Locate every blood parasite and identify its species.
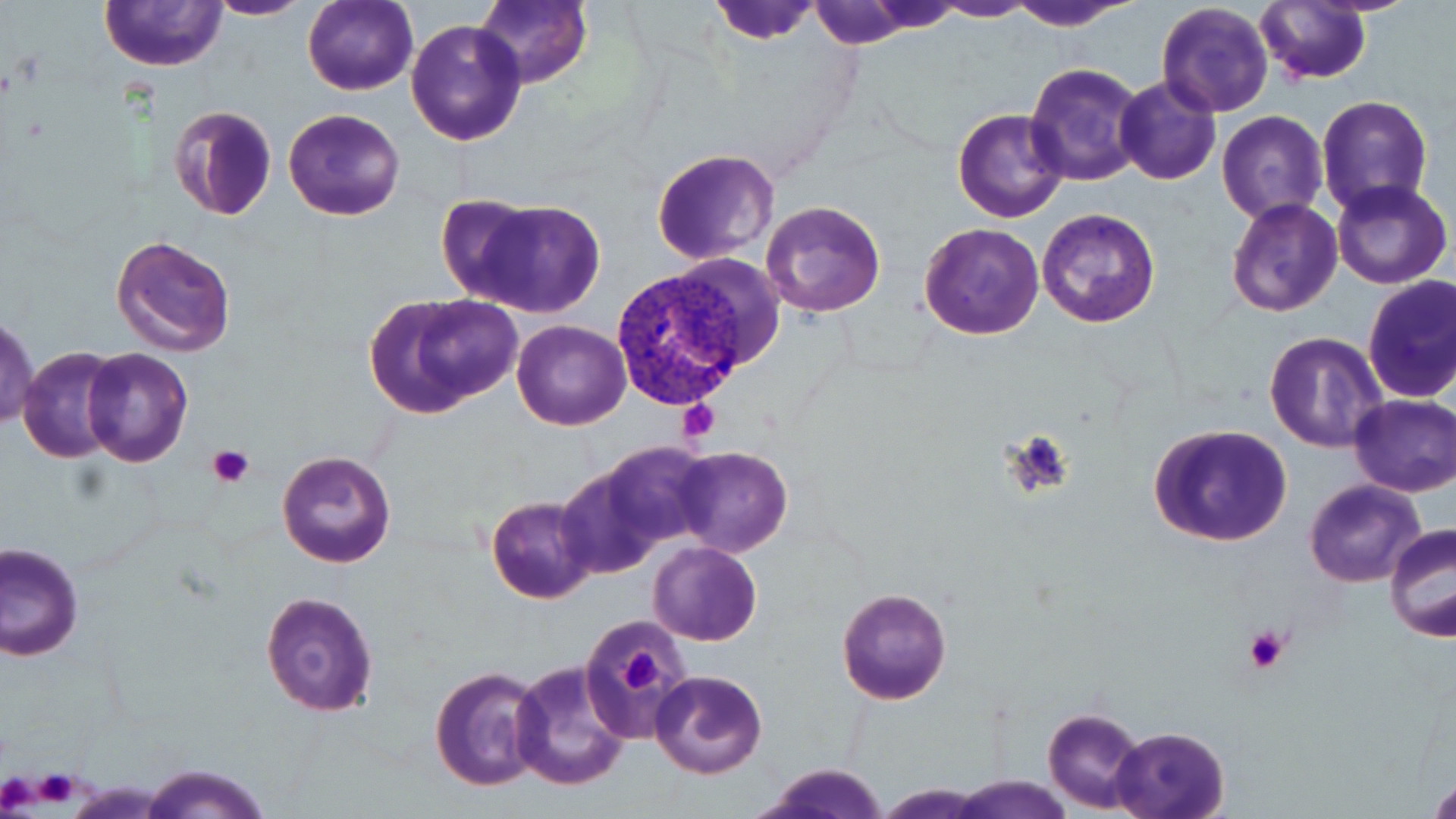

Approximate bounding boxes as named x1/y1/x2/y2 corners in pixels.
Plasmodium vivax-infected red blood cells: (x1=613, y1=267, x2=758, y2=412).
No Plasmodium falciparum, Plasmodium ovale, Plasmodium malariae, Babesia divergens, or Trypanosoma brucei observed.

Summary:
  - Uninfected red blood cell locations: (x1=101, y1=0, x2=227, y2=70), (x1=204, y1=0, x2=314, y2=20), (x1=302, y1=0, x2=417, y2=96), (x1=475, y1=0, x2=591, y2=90), (x1=705, y1=0, x2=822, y2=45), (x1=929, y1=0, x2=1039, y2=21), (x1=1005, y1=0, x2=1142, y2=31), (x1=807, y1=1, x2=919, y2=48), (x1=1256, y1=2, x2=1372, y2=86), (x1=1156, y1=3, x2=1274, y2=117), (x1=406, y1=19, x2=528, y2=147), (x1=1023, y1=63, x2=1147, y2=187), (x1=1115, y1=76, x2=1221, y2=186), (x1=976, y1=87, x2=1128, y2=210), (x1=1316, y1=95, x2=1434, y2=216), (x1=168, y1=104, x2=278, y2=221), (x1=953, y1=107, x2=1071, y2=223), (x1=284, y1=108, x2=404, y2=220), (x1=1217, y1=111, x2=1328, y2=226), (x1=651, y1=148, x2=780, y2=264), (x1=1331, y1=178, x2=1452, y2=289), (x1=436, y1=192, x2=544, y2=304), (x1=1226, y1=198, x2=1341, y2=317), (x1=760, y1=200, x2=887, y2=318), (x1=469, y1=201, x2=607, y2=317), (x1=1037, y1=208, x2=1161, y2=329), (x1=918, y1=221, x2=1044, y2=341), (x1=111, y1=234, x2=237, y2=357), (x1=659, y1=255, x2=783, y2=372), (x1=1362, y1=276, x2=1456, y2=403), (x1=362, y1=291, x2=517, y2=419), (x1=1, y1=316, x2=39, y2=429), (x1=513, y1=320, x2=631, y2=431), (x1=1264, y1=331, x2=1386, y2=453), (x1=19, y1=347, x2=125, y2=464), (x1=82, y1=347, x2=192, y2=467), (x1=1348, y1=394, x2=1456, y2=496), (x1=1148, y1=423, x2=1293, y2=547), (x1=597, y1=441, x2=715, y2=552), (x1=673, y1=446, x2=793, y2=558), (x1=277, y1=451, x2=396, y2=567), (x1=556, y1=464, x2=667, y2=579), (x1=1303, y1=478, x2=1427, y2=587), (x1=485, y1=496, x2=598, y2=604), (x1=1384, y1=523, x2=1456, y2=644), (x1=647, y1=541, x2=762, y2=646), (x1=2, y1=542, x2=82, y2=660), (x1=836, y1=587, x2=953, y2=705), (x1=259, y1=589, x2=381, y2=717), (x1=577, y1=614, x2=697, y2=747), (x1=509, y1=661, x2=632, y2=792), (x1=429, y1=665, x2=547, y2=792), (x1=649, y1=670, x2=768, y2=779), (x1=1041, y1=705, x2=1149, y2=812), (x1=1112, y1=725, x2=1230, y2=819), (x1=139, y1=763, x2=269, y2=819), (x1=750, y1=763, x2=893, y2=819), (x1=951, y1=774, x2=1072, y2=818), (x1=1429, y1=775, x2=1456, y2=817), (x1=877, y1=784, x2=991, y2=817)
  - Platelet locations: (x1=677, y1=400, x2=721, y2=442), (x1=1006, y1=433, x2=1077, y2=497), (x1=207, y1=445, x2=255, y2=487), (x1=1243, y1=626, x2=1292, y2=675), (x1=618, y1=646, x2=665, y2=696)
  - Slide-level diagnosis: Plasmodium vivax
  - Field of view: single
  - Stain: May-Grünwald-Giemsa
  - Image size: 1456×819 pixels
  - Magnification: 1000x
  - Preparation: thin blood film
  - Modality: optical microscopy